Give the extent of all Plasmodium falciparum-infected red blood cells.
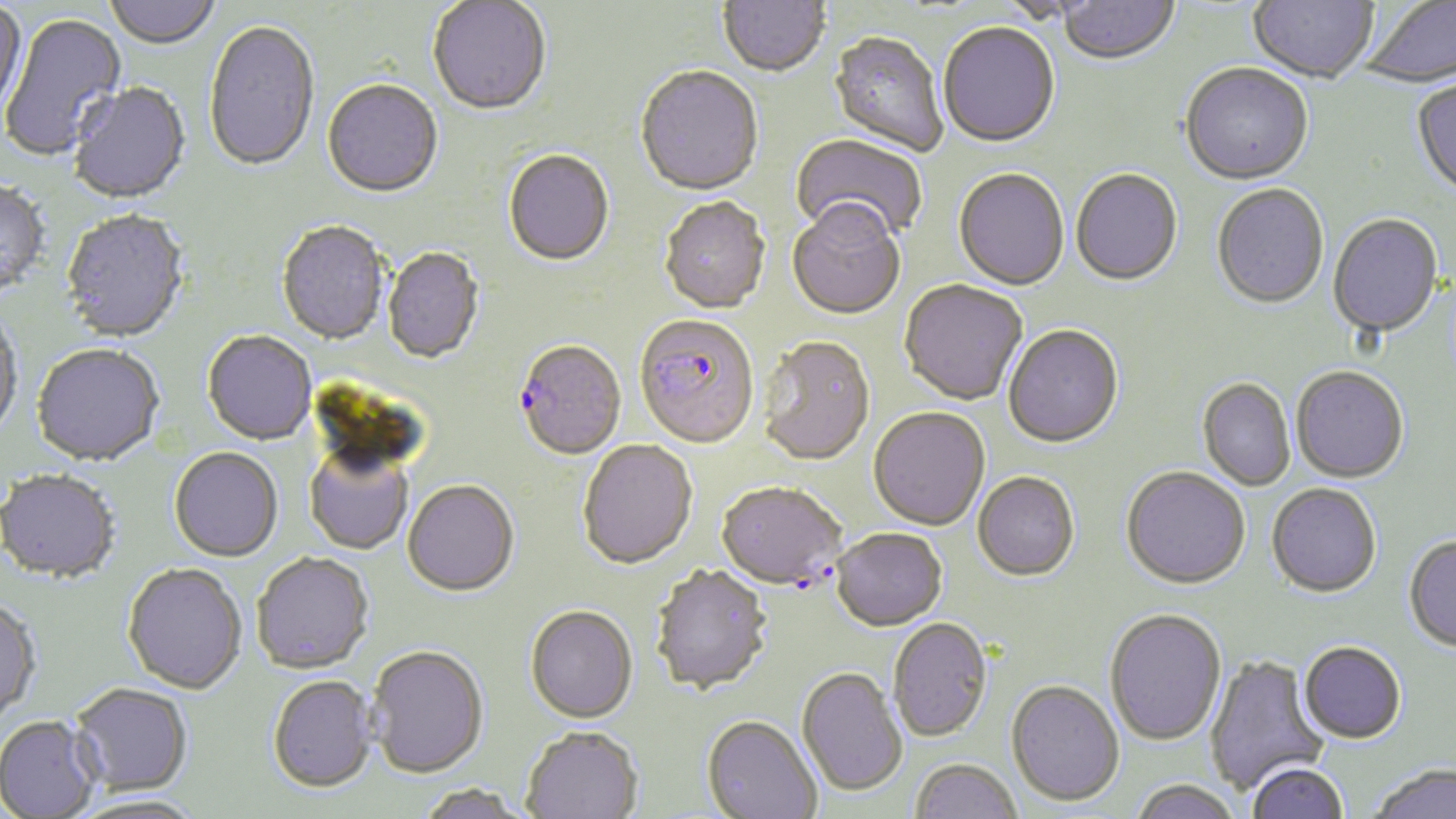

Approximate bounding boxes as [x1, y1, x2, y2] in pixels.
Plasmodium falciparum-infected red blood cells: [634, 316, 760, 451], [514, 342, 627, 463], [716, 484, 846, 591].

Uninfected red blood cell locations: [103, 0, 221, 51], [718, 0, 830, 80], [989, 0, 1107, 26], [1058, 0, 1180, 68], [1248, 0, 1377, 87], [1360, 0, 1456, 89], [427, 1, 551, 118], [0, 3, 27, 120], [2, 12, 127, 161], [204, 21, 320, 175], [938, 24, 1060, 150], [828, 33, 948, 157], [1180, 65, 1314, 188], [635, 68, 763, 199], [1411, 80, 1456, 202], [322, 81, 443, 200], [70, 83, 192, 206], [790, 133, 927, 249], [503, 151, 614, 268], [953, 170, 1069, 292], [1070, 171, 1183, 288], [0, 181, 51, 299], [1212, 185, 1329, 311], [659, 199, 771, 316], [787, 204, 905, 322], [59, 210, 190, 345], [1327, 215, 1444, 340], [276, 222, 390, 347], [382, 248, 483, 365], [899, 281, 1028, 407], [0, 310, 24, 443], [1003, 326, 1124, 450], [202, 332, 317, 446], [757, 339, 876, 468], [31, 345, 165, 469], [1291, 367, 1409, 484], [1197, 379, 1295, 491], [868, 408, 990, 532], [577, 441, 698, 571], [168, 448, 282, 563], [305, 448, 413, 555], [1121, 468, 1250, 591], [0, 471, 120, 586], [972, 473, 1080, 583], [403, 481, 519, 599], [1266, 483, 1381, 598], [831, 530, 948, 633], [1404, 536, 1456, 652], [252, 553, 374, 676], [123, 564, 248, 696], [650, 566, 773, 697], [0, 599, 42, 725], [524, 607, 638, 725], [1104, 610, 1226, 747], [888, 618, 993, 743], [1298, 642, 1407, 744], [366, 647, 489, 781], [1205, 654, 1329, 796], [796, 668, 907, 798], [267, 677, 377, 795], [1006, 681, 1124, 808], [69, 684, 193, 798], [701, 715, 822, 819], [0, 716, 101, 818], [520, 727, 643, 819], [909, 759, 1022, 819], [1247, 761, 1349, 819], [1369, 763, 1455, 819], [1129, 779, 1244, 819], [416, 783, 532, 819], [69, 794, 207, 819]. Slide-level diagnosis: Plasmodium falciparum. Light microscopy. 1000x magnification. Thin blood smear. One field of a larger specimen. May-Grünwald-Giemsa stain. Image is 1456×819 pixels.